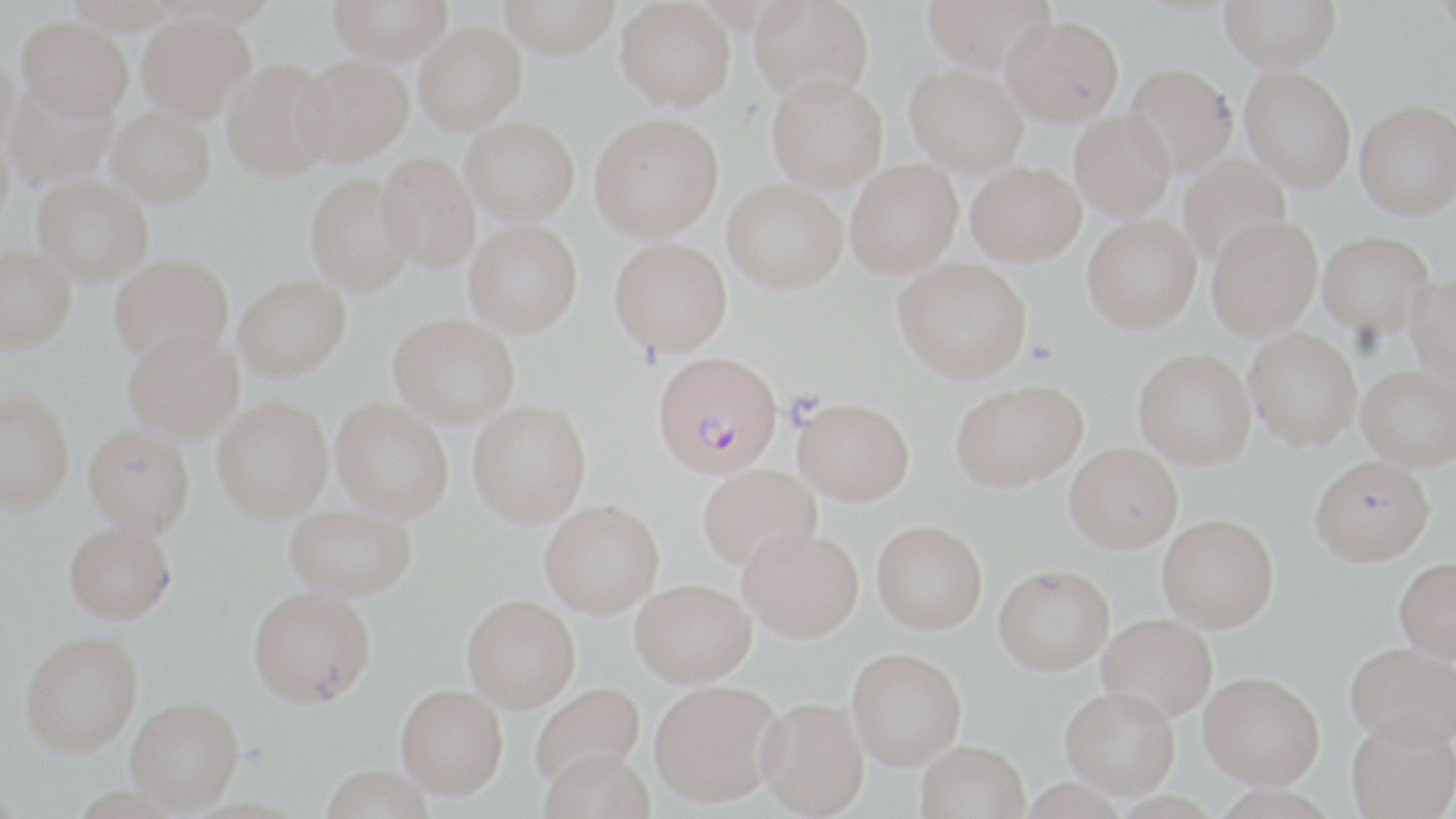
Approximate bounding boxes as (x1, y1, x2, y2) in pixels. Uninfected red blood cell locations: (66, 0, 181, 32), (328, 0, 452, 65), (498, 0, 620, 59), (616, 0, 735, 110), (749, 0, 873, 102), (922, 0, 1056, 74), (1220, 0, 1342, 72), (1434, 0, 1455, 48), (137, 11, 255, 122), (1001, 14, 1124, 126), (17, 16, 132, 121), (413, 22, 527, 133), (0, 53, 20, 157), (292, 56, 413, 166), (221, 58, 337, 181), (1123, 63, 1238, 178), (905, 64, 1028, 175), (1240, 66, 1356, 191), (766, 73, 888, 192), (4, 78, 118, 190), (1355, 100, 1455, 219), (106, 105, 216, 206), (1069, 111, 1176, 221), (589, 112, 724, 242), (461, 117, 580, 225), (0, 127, 14, 233), (376, 151, 481, 273), (1177, 154, 1292, 270), (845, 159, 963, 277), (967, 161, 1085, 265), (305, 173, 416, 295), (32, 177, 153, 284), (723, 179, 847, 293), (1206, 214, 1323, 339), (1082, 215, 1201, 333), (464, 219, 582, 336), (1318, 230, 1436, 338), (609, 238, 732, 356), (1, 245, 76, 351), (109, 254, 233, 365), (894, 258, 1032, 383), (234, 274, 350, 381), (1407, 275, 1456, 387), (389, 314, 520, 426), (122, 327, 244, 442), (1244, 328, 1363, 450), (1134, 349, 1256, 468), (1357, 364, 1456, 470), (951, 380, 1086, 491), (0, 389, 75, 512), (213, 395, 333, 522), (792, 397, 914, 505), (331, 399, 453, 520), (468, 400, 591, 527), (83, 424, 195, 536), (1065, 442, 1182, 552), (1310, 455, 1434, 565), (698, 464, 821, 572), (540, 501, 663, 617), (284, 502, 417, 599), (1157, 514, 1279, 631), (872, 520, 987, 633), (64, 521, 176, 623), (738, 526, 864, 642), (1394, 557, 1456, 662), (993, 564, 1115, 674), (630, 579, 757, 687), (248, 586, 376, 706), (462, 594, 580, 711), (1097, 613, 1217, 722), (19, 630, 143, 756), (1345, 642, 1456, 750), (846, 647, 966, 769), (1199, 671, 1325, 788), (650, 679, 783, 806), (530, 682, 645, 790), (396, 684, 508, 798), (1061, 686, 1180, 798), (126, 696, 244, 812), (756, 697, 869, 818), (1346, 719, 1456, 819), (916, 740, 1030, 819), (538, 748, 655, 819), (318, 765, 436, 819). Plasmodium falciparum-infected red blood cell locations: (652, 351, 783, 477). Slide-level diagnosis: Plasmodium falciparum. Captured at 1000x magnification. Thin blood smear. Image is 1456×819 pixels. Optical microscopy. May-Grünwald-Giemsa stain. Single field of view.